Give the position of every Plasmodium parasite visible.
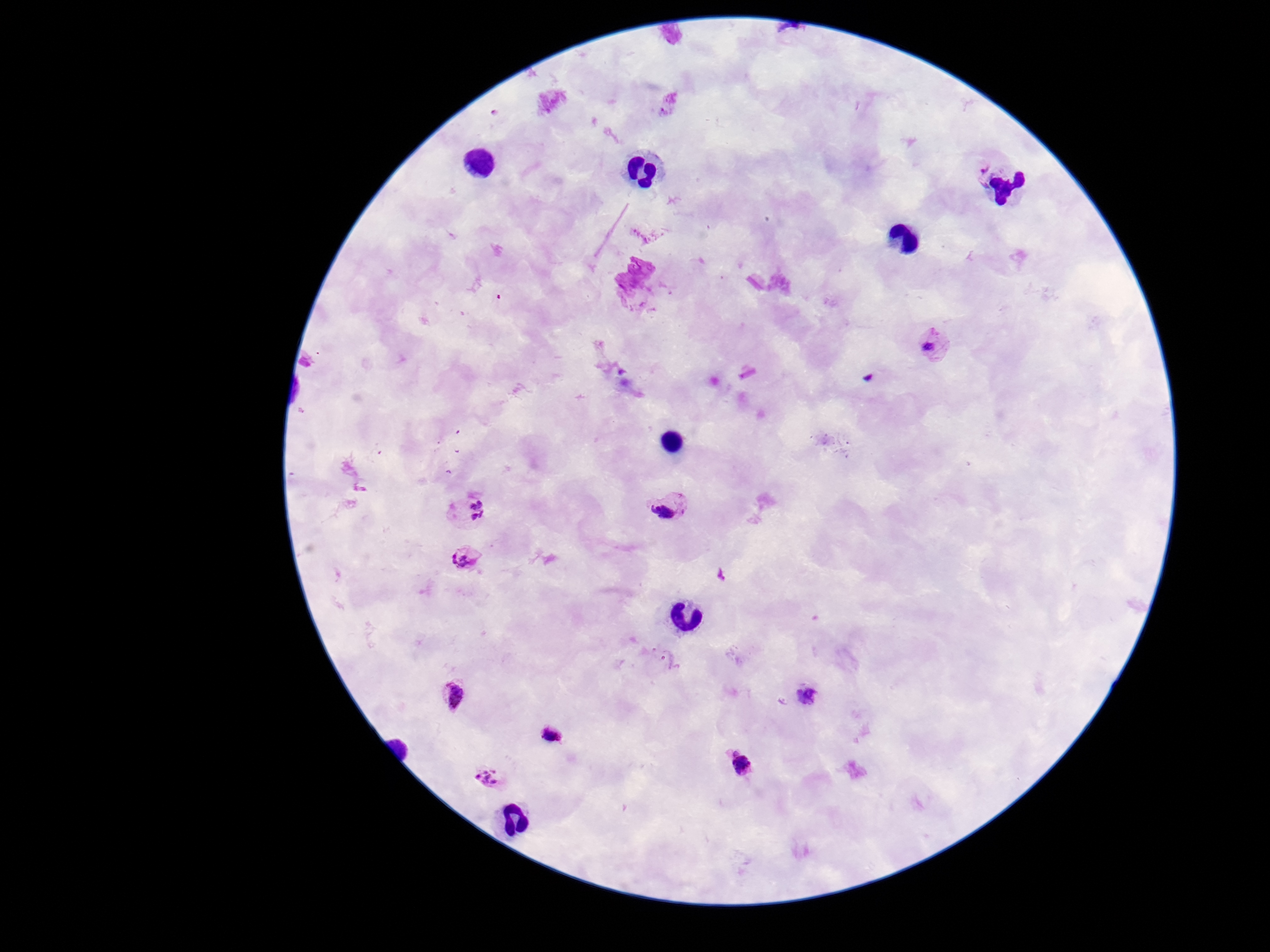
Approximate centers as [x, y] in pixels.
Plasmodium parasites: [972, 169], [934, 347], [670, 510], [468, 513], [466, 564], [806, 694], [451, 698], [555, 737], [736, 762], [490, 776].

Summary:
  - Image size: 1270×952 pixels
  - Field of view: one from this slide
  - Magnification: 100x
  - Preparation: thick blood film
  - Capture: smartphone camera through the microscope eyepiece
  - Stain: Giemsa
  - Patient malaria status: infected